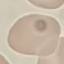

Summary:
  - Result: no malaria parasites detected
  - Preparation: thin blood smear
  - Capture: smartphone camera at the microscope eyepiece
  - Image type: cell patch, automatically extracted from a larger field of view and resized to 64 × 64 pixels
  - Stain: Giemsa